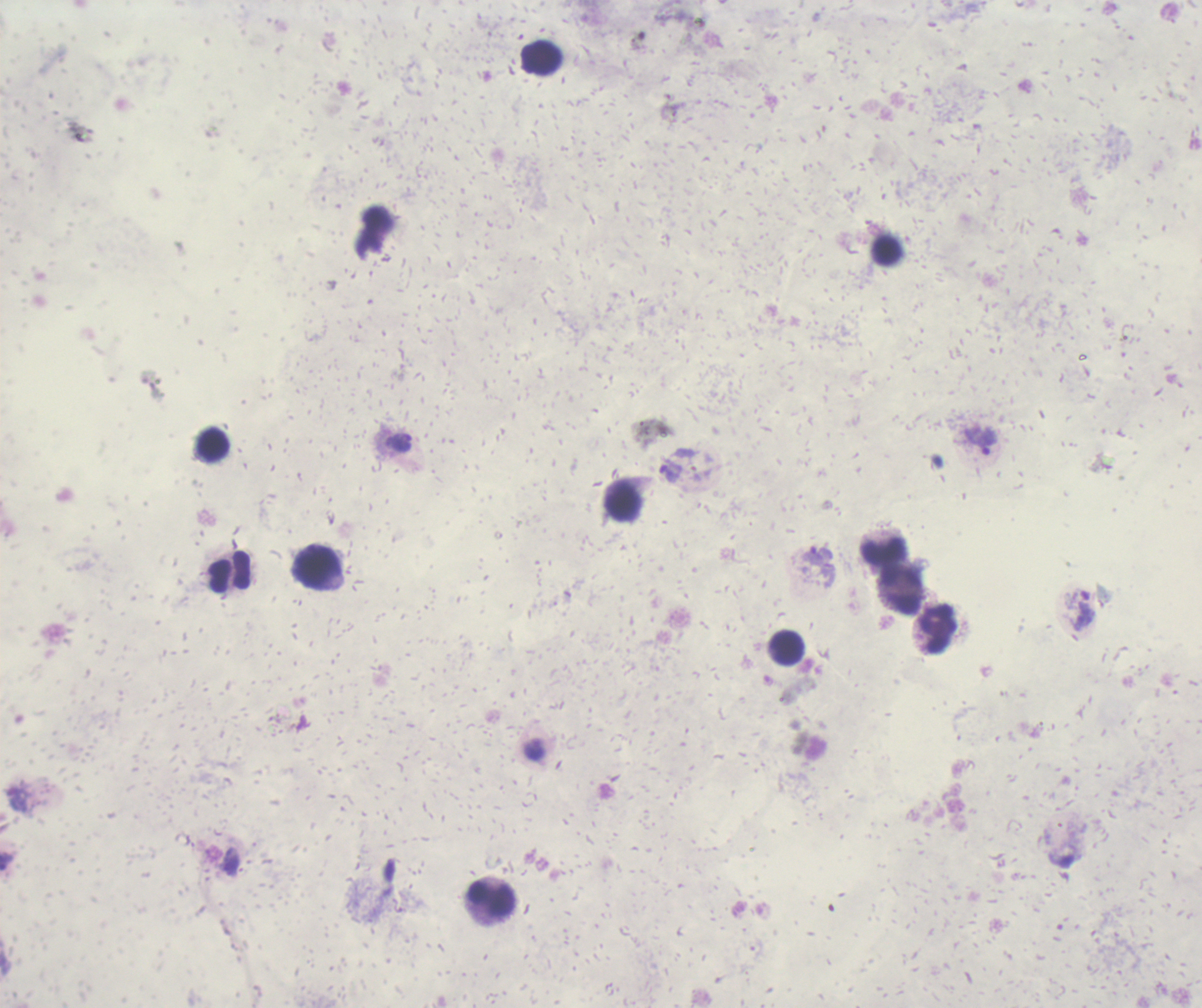

Approximate centers as [x, y] in pixels.
Summary:
  - Gametocyte locations: [810, 746]
  - Leukocyte locations: [541, 58], [213, 445], [623, 503], [884, 552], [317, 568], [230, 572], [902, 592], [938, 630], [788, 647], [492, 900]
  - Trophozoite locations: [980, 441], [399, 443], [817, 557], [1084, 616]
  - Life-cycle stages observed: trophozoite, gametocyte
  - Coloration quality: bad
  - Context: previously used in an actual diagnosis
  - Background quality: unsatisfactory
  - Image size: 1202×1008 pixels
  - Magnification: 100x
  - Preparation: thick blood smear
  - Result: malaria parasites detected
  - Stain: Romanowsky
  - Field of view: single